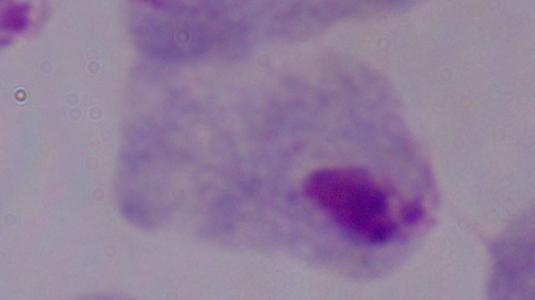
Summary:
  - Magnification: 1000x
  - Identification: trichomonad
  - Modality: micrograph